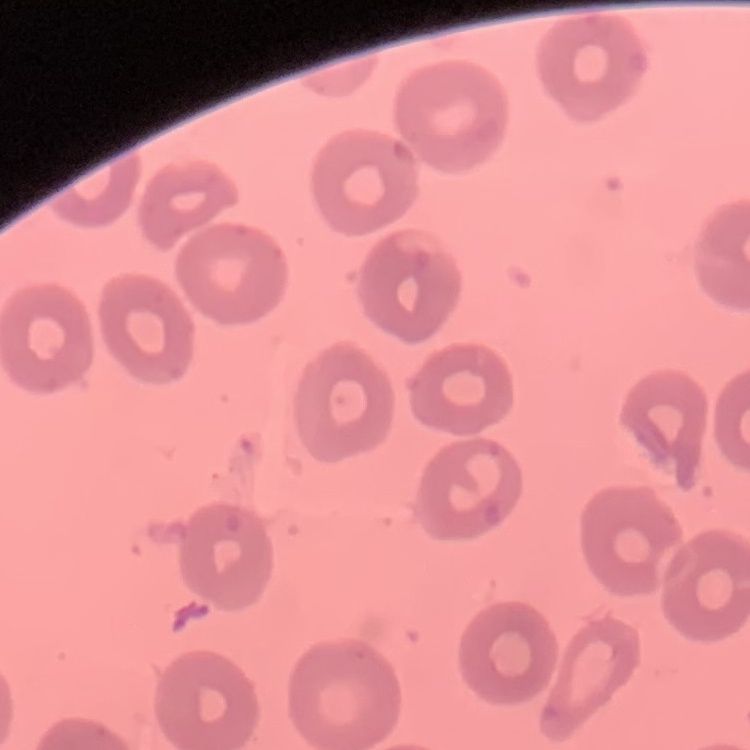

Summary:
  - Red blood cell morphology: no rouleaux formation
  - Stain: Field's or Giemsa
  - Preparation: thin peripheral smear
  - Image type: square crop of a larger photomicrograph